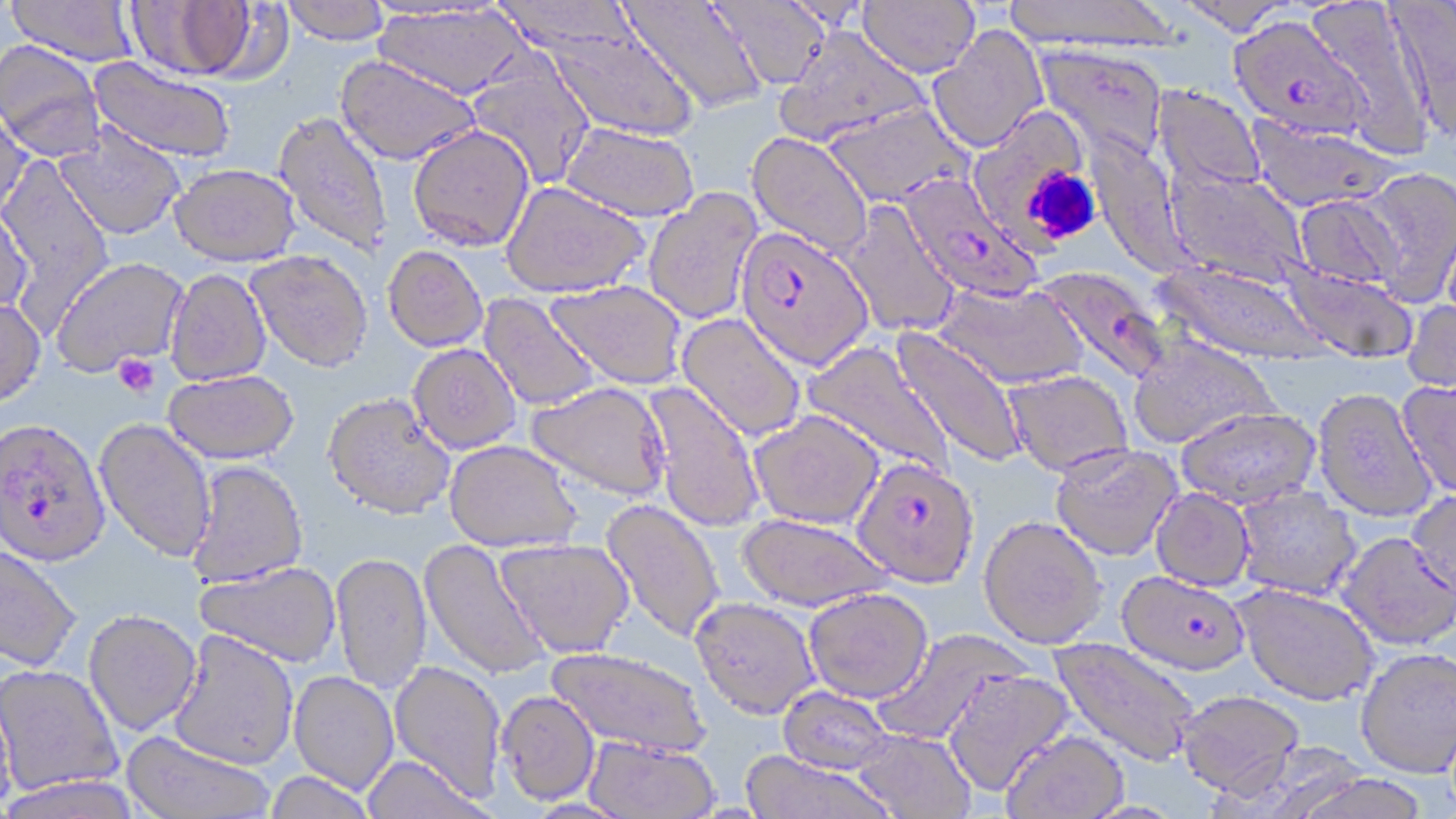 Approximate bounding boxes as (x1, y1, x2, y2) in pixels. Platelet locations: (1035, 171, 1097, 240), (113, 353, 160, 397). Uninfected red blood cell locations: (6, 0, 139, 67), (281, 0, 389, 44), (858, 0, 979, 77), (1002, 0, 1178, 49), (1175, 0, 1297, 36), (127, 1, 256, 80), (620, 1, 768, 114), (492, 2, 656, 54), (710, 2, 832, 90), (1387, 2, 1456, 145), (1309, 3, 1433, 156), (374, 4, 529, 100), (525, 16, 699, 143), (927, 25, 1049, 153), (772, 26, 930, 147), (0, 40, 106, 160), (1035, 44, 1168, 161), (466, 51, 597, 189), (335, 55, 481, 165), (88, 56, 236, 164), (1153, 83, 1266, 195), (822, 101, 974, 208), (0, 106, 34, 222), (977, 110, 1085, 256), (272, 111, 394, 259), (1245, 115, 1399, 214), (560, 121, 699, 222), (54, 123, 186, 240), (407, 124, 534, 250), (747, 131, 873, 259), (0, 155, 115, 326), (169, 163, 300, 266), (1165, 167, 1310, 286), (1356, 169, 1456, 305), (501, 181, 650, 297), (643, 188, 764, 325), (1293, 192, 1408, 294), (0, 201, 33, 319), (838, 201, 961, 338), (382, 245, 488, 351), (247, 250, 373, 372), (50, 257, 189, 377), (1157, 260, 1331, 366), (1281, 263, 1418, 364), (165, 268, 271, 385), (545, 279, 686, 389), (933, 282, 1088, 389), (479, 293, 603, 411), (0, 297, 46, 406), (1402, 297, 1456, 398), (676, 312, 807, 443), (892, 326, 1029, 468), (1127, 334, 1280, 449), (804, 340, 957, 481), (409, 343, 521, 453), (163, 369, 298, 464), (1004, 369, 1134, 476), (1396, 378, 1456, 500), (643, 380, 765, 532), (526, 382, 671, 500), (1312, 388, 1437, 522), (323, 392, 455, 519), (1175, 406, 1321, 508), (748, 409, 884, 529), (94, 418, 217, 561), (444, 440, 582, 552), (1050, 442, 1183, 561), (186, 460, 308, 588), (1234, 485, 1362, 599), (1151, 488, 1255, 591), (1406, 489, 1456, 601), (600, 499, 725, 643), (738, 513, 894, 612), (978, 514, 1107, 648), (1336, 530, 1455, 650), (495, 538, 634, 658), (419, 539, 548, 681), (0, 541, 82, 672), (330, 552, 432, 694), (195, 560, 342, 668), (1233, 581, 1380, 706), (804, 588, 933, 703), (691, 597, 820, 719), (83, 609, 202, 736), (168, 628, 298, 770), (873, 629, 1029, 747), (1050, 636, 1202, 766), (546, 646, 711, 757), (1355, 647, 1456, 777), (389, 660, 507, 800), (0, 665, 123, 797), (942, 668, 1075, 797), (289, 671, 399, 794), (0, 679, 17, 815), (777, 686, 895, 774), (1175, 688, 1305, 798), (497, 690, 600, 805), (850, 729, 976, 819), (121, 730, 274, 819), (1001, 730, 1129, 819), (584, 736, 719, 818), (739, 751, 897, 819), (360, 755, 492, 819), (263, 770, 378, 819), (1291, 774, 1432, 819). Plasmodium falciparum-infected red blood cell locations: (1230, 15, 1373, 140), (899, 174, 1042, 303), (735, 226, 874, 370), (1047, 264, 1167, 382), (0, 417, 110, 565), (852, 457, 980, 588), (1117, 570, 1251, 675). Slide-level diagnosis: Plasmodium falciparum. Light microscopy. May-Grünwald-Giemsa-stained preparation. Single field of view. Thin blood film. Image is 1456×819 pixels. 1000x magnification.